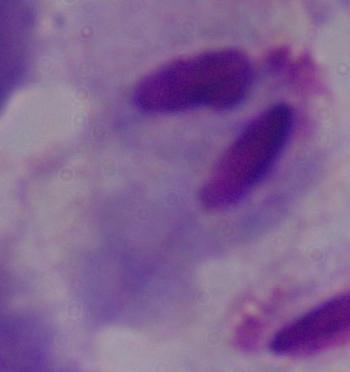
Summary:
  - Modality: micrograph
  - Identification: trichomonad
  - Magnification: 1000x